Comment on the morphology of the erythrocytes.
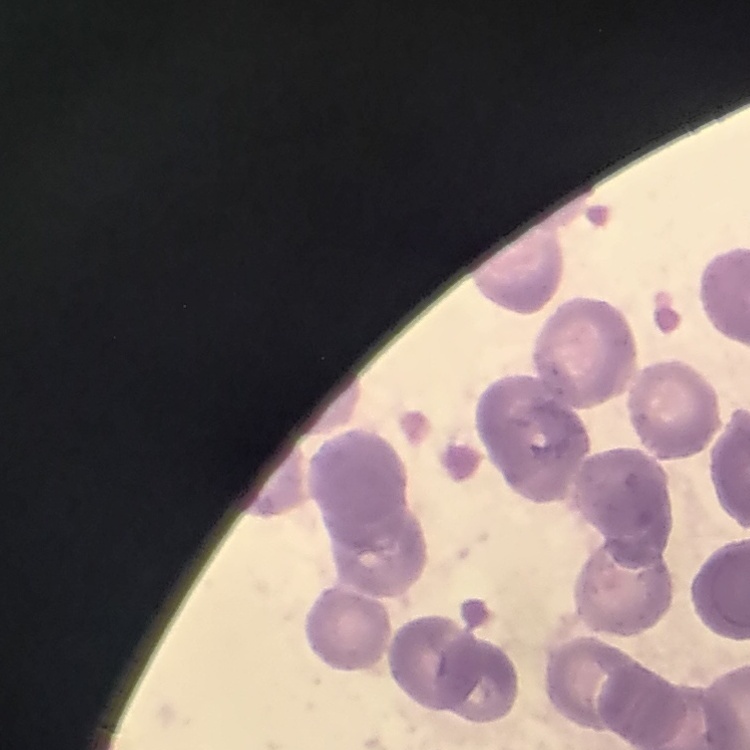

Rouleaux formation.

Summary:
  - Preparation: thin blood film
  - Image type: one tile cut from a larger photomicrograph
  - Stain: Field's or Giemsa